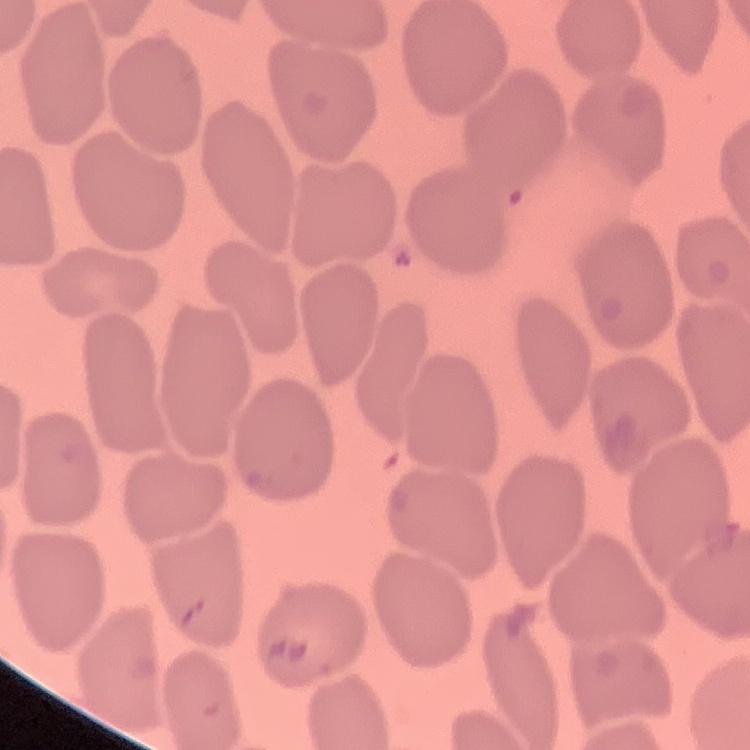
{
  "red_blood_cell_morphology": "no rouleaux formation",
  "stain": "Field's or Giemsa",
  "preparation": "thin peripheral smear",
  "image_type": "one tile cut from a larger photomicrograph"
}